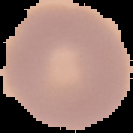 Image is 133×133 pixels. From a thin blood smear. The area outside the segmented cell region is set to black. Result: no Plasmodium parasites detected.